Locate malaria parasites and identify their life-cycle stages.
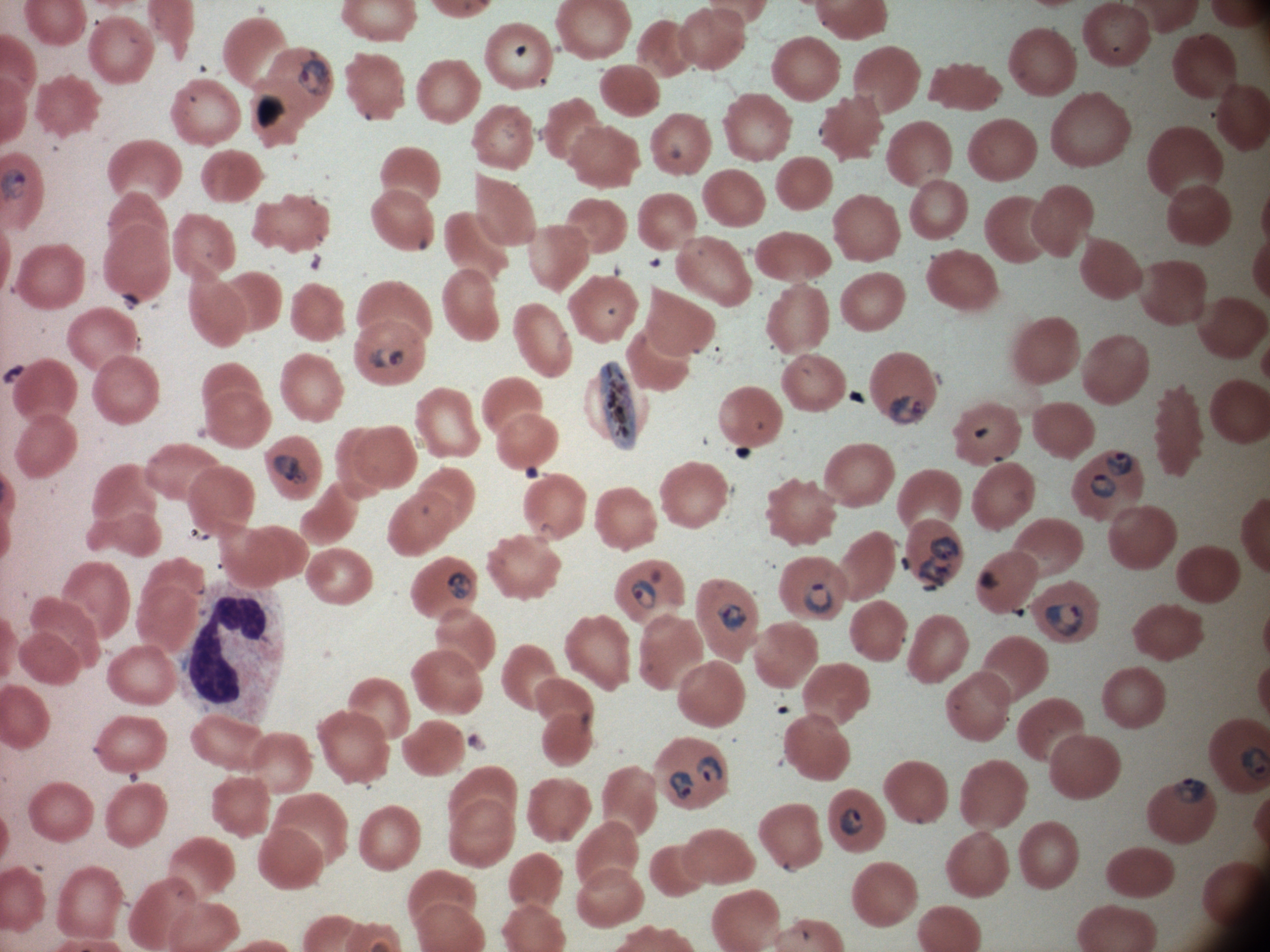

Approximate bounding boxes as named x1/y1/x2/y2 corners in pixels, from the source annotation, which is not necessarily exhaustive.
Ring forms: (x1=1105, y1=451, x2=1133, y2=476), (x1=1090, y1=473, x2=1116, y2=500), (x1=631, y1=578, x2=658, y2=609), (x1=802, y1=580, x2=835, y2=616), (x1=1043, y1=602, x2=1084, y2=637), (x1=1172, y1=777, x2=1208, y2=806), (x1=839, y1=807, x2=864, y2=838).
Trophozoites: (x1=296, y1=50, x2=332, y2=97), (x1=369, y1=346, x2=406, y2=371), (x1=889, y1=395, x2=927, y2=425), (x1=273, y1=454, x2=308, y2=486), (x1=930, y1=534, x2=961, y2=563), (x1=917, y1=555, x2=954, y2=587), (x1=447, y1=571, x2=473, y2=599), (x1=715, y1=603, x2=747, y2=633), (x1=694, y1=756, x2=723, y2=784), (x1=668, y1=770, x2=695, y2=801).
Gametocytes: (x1=598, y1=358, x2=638, y2=453).

Summary:
  - Life-cycle stages among the annotated parasites: ring form, trophozoite, gametocyte
  - Stain: Giemsa
  - Magnification: 100x
  - Preparation: thin blood film
  - Field of view: single
  - Microscope: Leica DM2000 with built-in camera
  - Image size: 1270×952 pixels
  - Species: Plasmodium falciparum